Identify the cell.
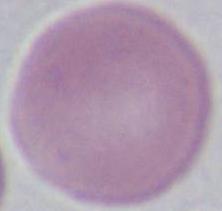

An erythrocyte.

Summary:
  - Modality: micrograph
  - Magnification: 1000x